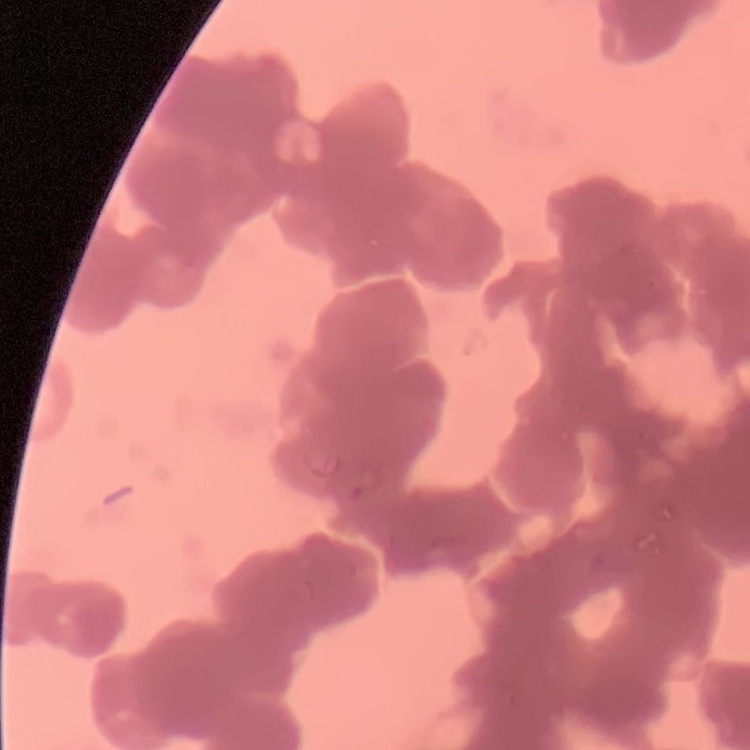

red blood cell morphology = rouleaux formation
stain = Field's or Giemsa
preparation = thin peripheral smear
image type = one tile cut from a larger photomicrograph